Assess this cell for malaria.
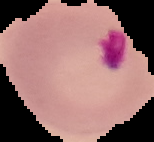
Uninfected.

Segmented cell region on a black background. Image is 154×142 pixels. From a thin blood film.